Report the malaria status of this cell.
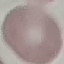
Uninfected.

stain = Giemsa
image type = automatically extracted cell patch, resized to 64 × 64 pixels
preparation = thin blood film
capture = smartphone through the microscope eyepiece